Give the position of every Plasmodium parasite visible.
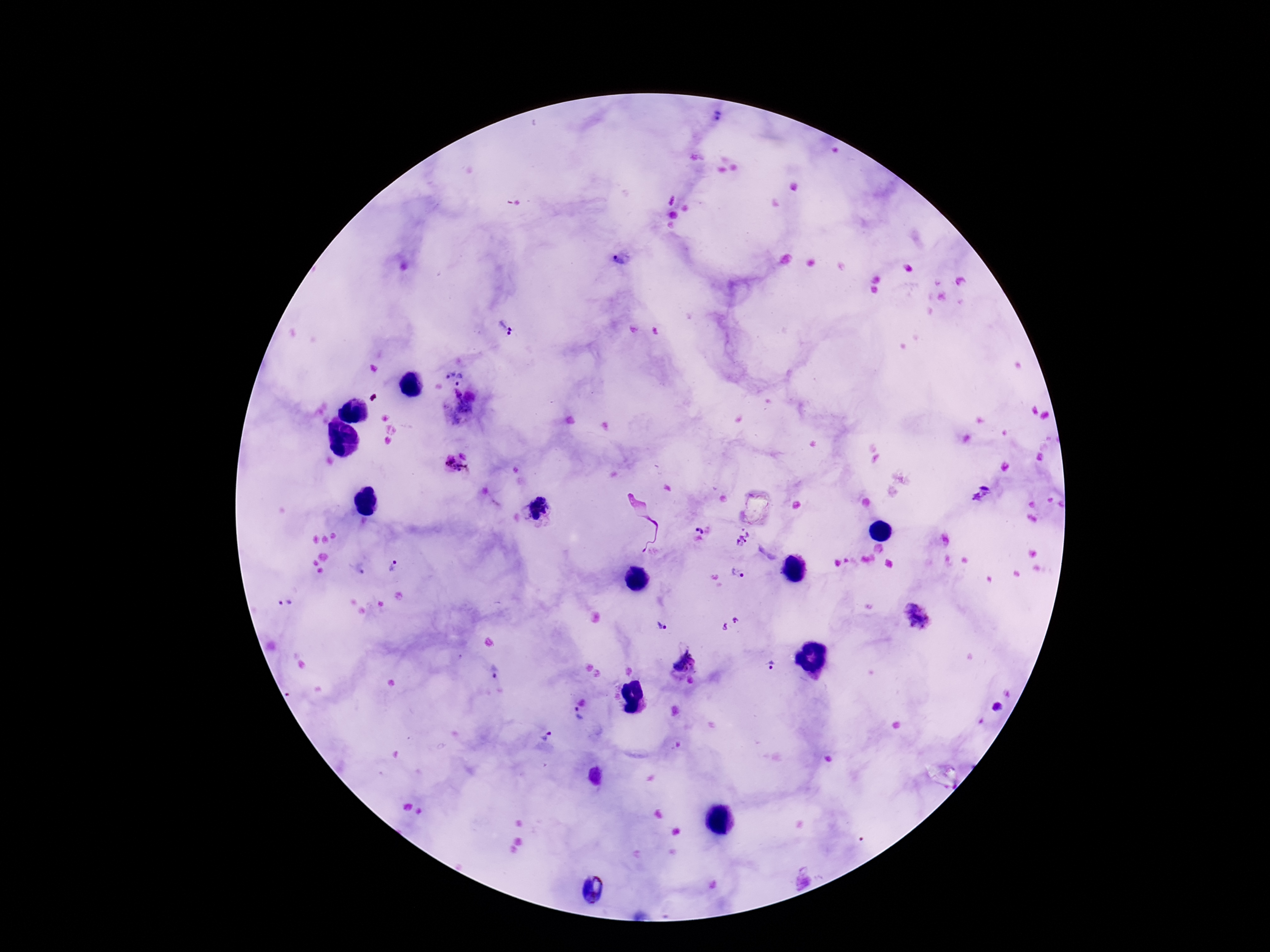
Approximate object centers, in pixels from the top-left corner.
Plasmodium parasites: (x=718, y=121), (x=621, y=259), (x=506, y=324), (x=449, y=373), (x=462, y=380), (x=461, y=409), (x=456, y=463), (x=981, y=493), (x=539, y=508), (x=698, y=529), (x=744, y=537), (x=394, y=567), (x=739, y=574), (x=286, y=604), (x=917, y=618), (x=731, y=624), (x=662, y=626), (x=685, y=664), (x=774, y=664), (x=493, y=672), (x=578, y=717), (x=546, y=735), (x=593, y=891).

Smartphone photograph taken through the microscope eyepiece. Thick peripheral-blood smear. Image is 1270×952 pixels. Patient malaria status: positive. Giemsa stain. 100x magnification. Single field of view.